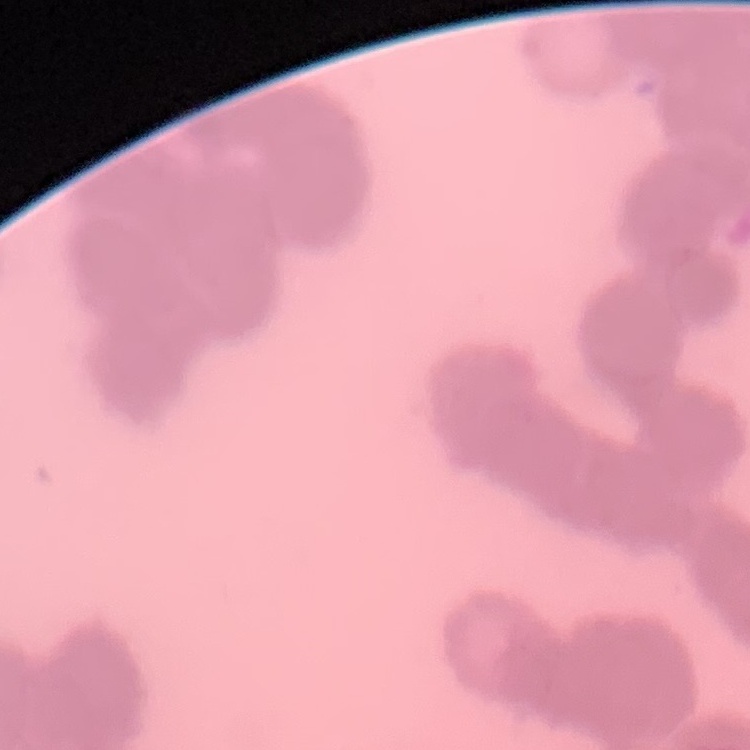
Summary:
  - Erythrocyte morphology: rouleaux formation
  - Image type: square crop of a larger photomicrograph
  - Stain: Field's or Giemsa
  - Preparation: thin peripheral smear